Classify this cell by malaria status.
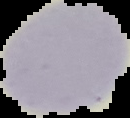

It is uninfected.

Image is 130×118 pixels. The area outside the segmented cell region is set to black. From a thin blood smear.